Classify this cell by malaria status.
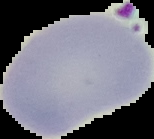

Uninfected.

Image is 154×139 pixels. From a thin blood film. Segmented cell region on a black background.